State which parasite is depicted.
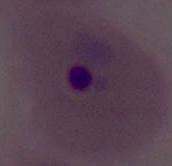

Plasmodium.

magnification = 400x or 1000x
modality = micrograph